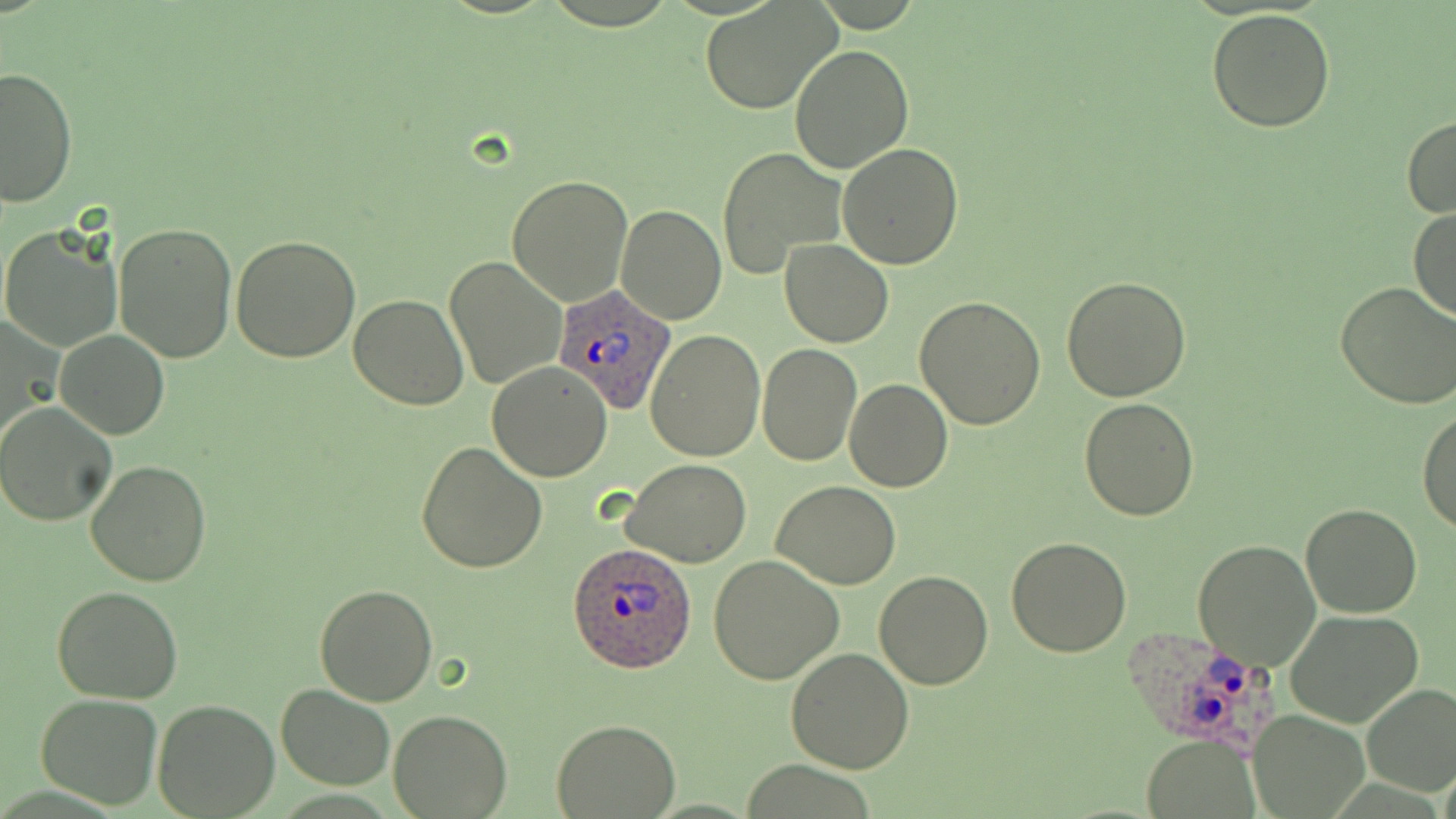
Approximate bounding boxes as [x1, y1, x2, y2] in pixels. Plasmodium ovale-infected red blood cell locations: [552, 283, 677, 415], [566, 543, 698, 673], [1122, 624, 1287, 745]. Uninfected red blood cell locations: [699, 1, 838, 114], [1205, 9, 1337, 132], [734, 21, 893, 154], [790, 43, 913, 174], [1, 66, 77, 209], [1402, 117, 1456, 218], [837, 141, 964, 268], [719, 147, 845, 279], [506, 174, 635, 306], [616, 204, 726, 325], [1407, 208, 1455, 323], [114, 222, 238, 363], [0, 226, 122, 353], [231, 234, 360, 362], [779, 239, 894, 347], [444, 255, 567, 392], [1061, 276, 1192, 403], [1334, 281, 1456, 409], [349, 293, 469, 409], [914, 297, 1046, 430], [0, 316, 59, 447], [55, 330, 169, 440], [645, 330, 765, 461], [756, 343, 861, 466], [487, 361, 614, 481], [844, 378, 952, 493], [1078, 397, 1199, 520], [0, 403, 118, 526], [1418, 405, 1456, 536], [417, 440, 548, 574], [84, 459, 213, 588], [621, 459, 750, 568], [770, 480, 901, 589], [1300, 502, 1421, 618], [1006, 537, 1133, 658], [1194, 538, 1322, 670], [708, 555, 843, 684], [874, 570, 993, 690], [53, 583, 184, 702], [315, 583, 438, 705], [1283, 610, 1424, 729], [786, 646, 914, 774], [1360, 684, 1456, 796], [275, 685, 396, 790], [35, 693, 162, 808], [273, 697, 513, 803], [152, 700, 280, 818], [389, 709, 511, 818], [1248, 709, 1369, 817], [550, 719, 680, 817], [1142, 735, 1259, 816]. Slide-level diagnosis: Plasmodium ovale. Light microscopy. Thin blood smear. May-Grünwald-Giemsa stain. Single field of view. Image is 1456×819 pixels. Captured at 1000x magnification.